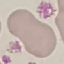
result = no malaria parasites seen
capture = smartphone through the microscope eyepiece
stain = Giemsa
preparation = thin blood film
image type = automatically extracted cell patch, resized to 64 × 64 pixels